Classify this cell by malaria status.
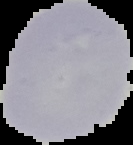
It is uninfected.

preparation: thin blood film
image_size: 133×145 pixels
image_type: segmented cell region on a black background